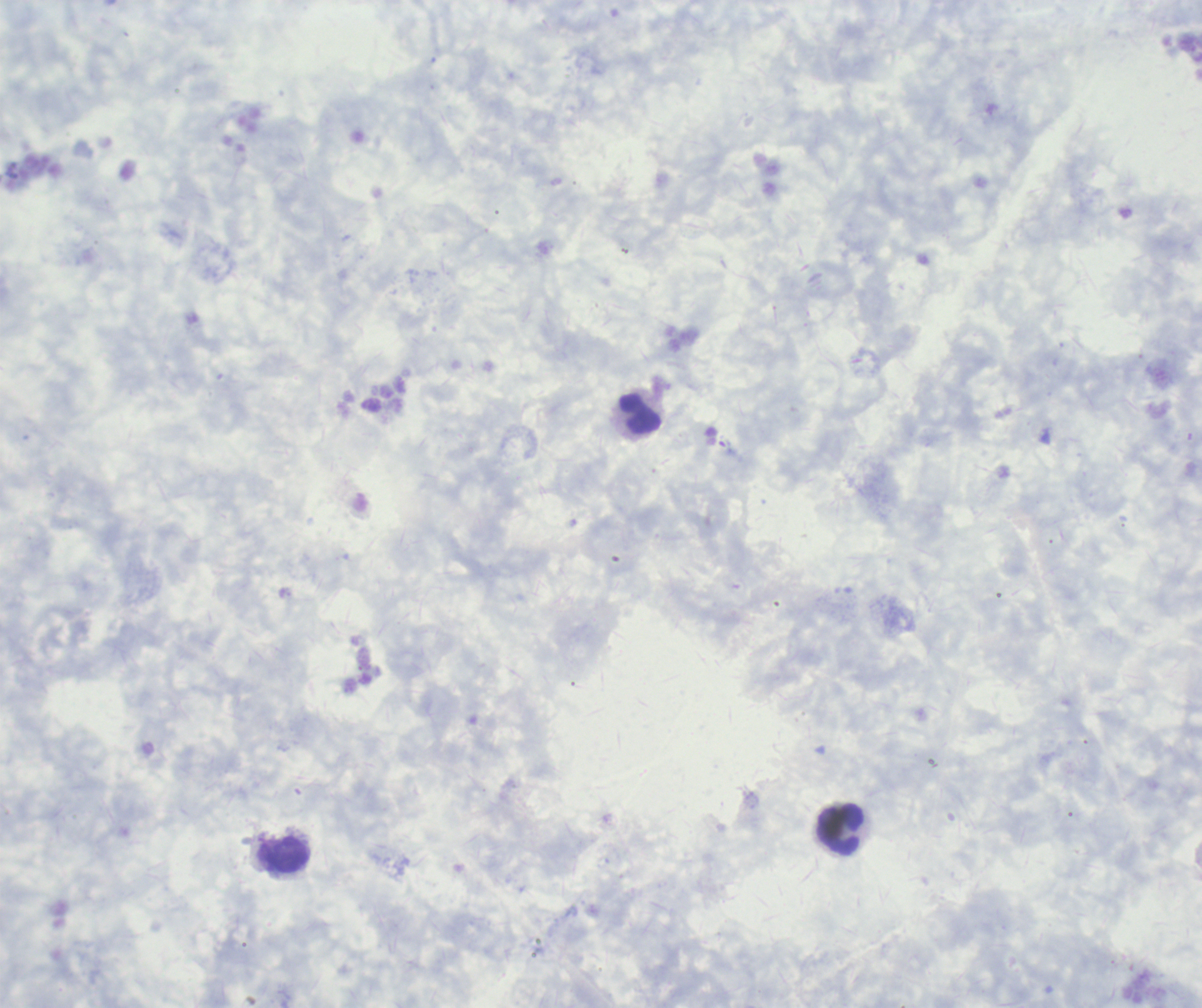

coordinate format = approximate object centers, in pixels from the top-left corner
leukocyte locations = (x=641, y=413), (x=841, y=829), (x=283, y=855)
stain = Romanowsky
background quality = poor
context = previously used in a real diagnosis
magnification = 100x
image size = 1202×1008 pixels
result = no malaria parasites detected
field of view = single
preparation = thick blood film
coloration quality = good